State which parasite is depicted.
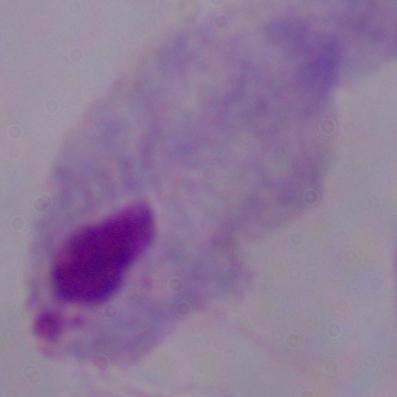
A trichomonad.

Photomicrograph. Captured at 1000x magnification.